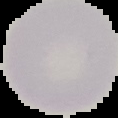
Summary:
  - Preparation: thin blood film
  - Malaria status: uninfected
  - Image size: 118×118 pixels
  - Image type: cell region segmented out of the field of view; surrounding area masked to black